Describe the morphology of the red blood cells.
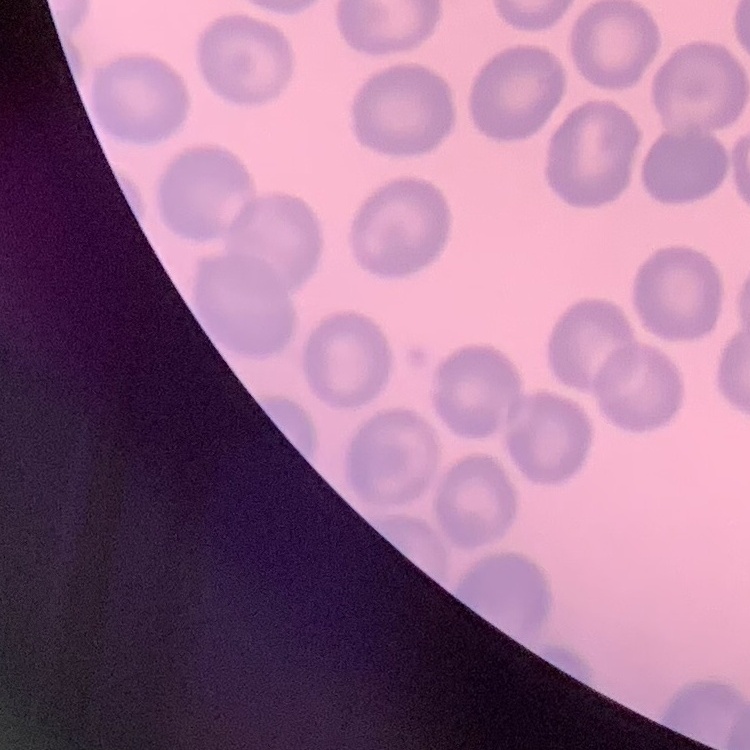
No rouleaux formation.

Summary:
  - Preparation: thin blood film
  - Image type: one tile cut from a larger photomicrograph
  - Stain: Field's or Giemsa